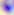
400x magnification. Toxoplasma gondii is shown. Photomicrograph.